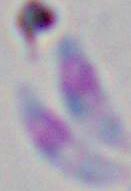
magnification = 1000x
identification = Toxoplasma gondii
modality = micrograph